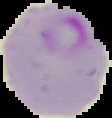

malaria status = parasitized
image type = cell region segmented out of the field of view; surrounding area masked to black
preparation = thin blood smear
image size = 112×118 pixels